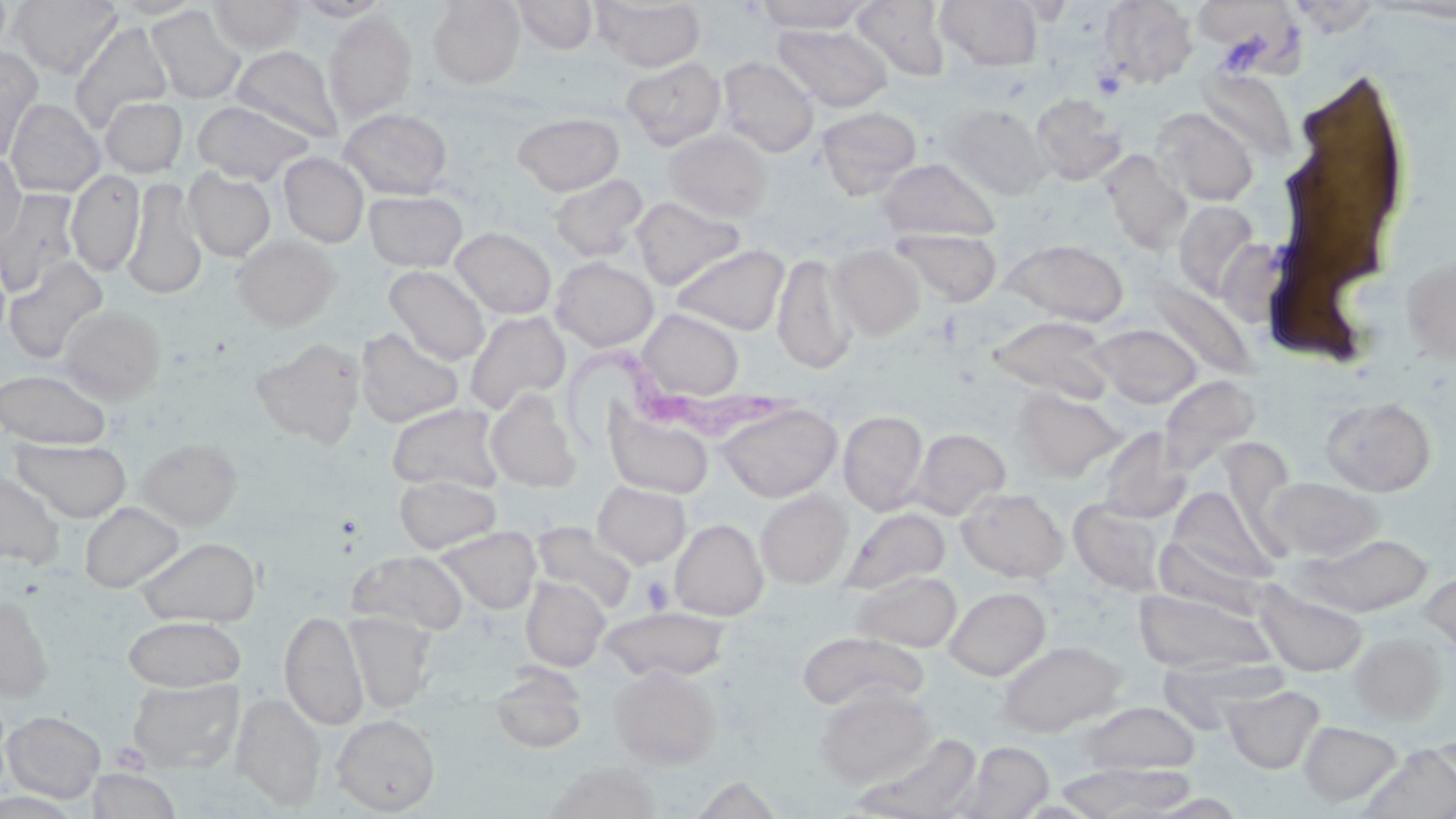
slide_level_diagnosis: Trypanosoma brucei
stain: May-Grünwald-Giemsa
field_of_view: one of a larger specimen
platelet_locations: 'approximate bounding boxes as [x1, y1, x2, y2] in pixels: [1092, 68, 1126, 100], [641, 576, 674, 613]'
magnification: 1000x
uninfected_red_blood_cell_locations: 'approximate bounding boxes as [x1, y1, x2, y2] in pixels: [10, 0, 122, 78], [107, 0, 207, 18], [208, 0, 305, 54], [290, 0, 393, 21], [427, 0, 525, 88], [513, 0, 598, 54], [593, 0, 706, 72], [754, 0, 870, 32], [936, 0, 1043, 71], [1097, 0, 1198, 88], [1201, 0, 1308, 81], [852, 1, 951, 81], [146, 6, 245, 104], [324, 11, 418, 122], [70, 20, 172, 130], [773, 23, 892, 112], [230, 44, 343, 144], [0, 47, 43, 162], [717, 56, 819, 157], [621, 57, 726, 149], [1286, 57, 1410, 296], [1196, 67, 1299, 163], [1031, 92, 1127, 185], [100, 96, 187, 177], [4, 98, 105, 197], [192, 100, 313, 184], [942, 103, 1052, 199], [816, 106, 922, 197], [1151, 107, 1259, 206], [339, 108, 453, 199], [513, 113, 624, 196], [664, 130, 773, 223], [1101, 151, 1193, 254], [0, 152, 26, 245], [279, 153, 368, 247], [877, 157, 1000, 242], [183, 168, 275, 261], [66, 170, 145, 276], [550, 174, 649, 262], [123, 178, 207, 300], [0, 189, 80, 296], [372, 189, 472, 361], [365, 190, 467, 271], [631, 196, 745, 290], [1173, 200, 1261, 300], [450, 227, 556, 319], [893, 228, 1002, 306], [231, 235, 340, 331], [1002, 238, 1129, 326], [670, 243, 789, 335], [829, 244, 925, 340], [773, 253, 857, 375], [1401, 253, 1456, 367], [4, 257, 108, 363], [551, 257, 658, 351], [385, 265, 490, 365], [1148, 282, 1256, 379], [59, 304, 165, 403], [637, 309, 744, 400], [464, 311, 570, 414], [986, 314, 1115, 405], [1093, 323, 1201, 409], [355, 327, 464, 427], [250, 338, 366, 448], [0, 368, 112, 449], [1158, 376, 1261, 477], [1011, 388, 1125, 482], [485, 389, 581, 492], [1320, 396, 1436, 496], [387, 402, 504, 493], [718, 403, 841, 502], [604, 405, 714, 499], [838, 410, 928, 516], [1097, 427, 1191, 524], [910, 428, 1010, 520], [11, 438, 131, 522], [137, 438, 242, 529], [0, 470, 65, 568], [394, 475, 502, 553], [1262, 476, 1384, 561], [593, 482, 691, 567], [1166, 486, 1276, 585], [957, 487, 1068, 582], [756, 490, 852, 589], [1068, 498, 1169, 595], [80, 502, 184, 592], [840, 507, 949, 595], [670, 518, 768, 620], [531, 522, 638, 614], [437, 527, 541, 613], [1299, 533, 1433, 616], [134, 536, 261, 627], [349, 550, 468, 635], [1420, 568, 1456, 657], [851, 570, 962, 652], [520, 577, 609, 671], [1255, 585, 1367, 677], [944, 586, 1051, 680], [1132, 588, 1276, 674], [0, 596, 54, 700], [602, 607, 729, 682], [279, 609, 368, 730], [345, 612, 438, 713], [123, 616, 245, 690], [799, 632, 927, 712], [1348, 633, 1446, 725], [997, 640, 1126, 737], [609, 665, 722, 769], [488, 666, 588, 752], [126, 678, 243, 773], [1222, 684, 1325, 773], [815, 685, 936, 788], [233, 692, 326, 810], [1079, 701, 1200, 776], [3, 710, 106, 803], [331, 714, 440, 815], [1298, 720, 1402, 806], [855, 732, 982, 819], [952, 741, 1054, 819], [1358, 743, 1456, 819], [543, 761, 664, 819], [1055, 761, 1197, 818], [87, 768, 182, 819]'
preparation: thin blood film
image_size: 1456×819 pixels
modality: optical microscopy
trypanosoma_brucei_locations: 'approximate bounding boxes as [x1, y1, x2, y2] in pixels: [536, 328, 806, 457]'